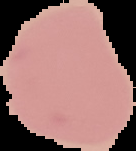

Image is 136×151 pixels. From a thin blood smear. Segmented cell region on a black background. Malaria status: uninfected.